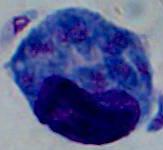

magnification = 1000x
identification = leukocyte
modality = micrograph